Give the preparation type.
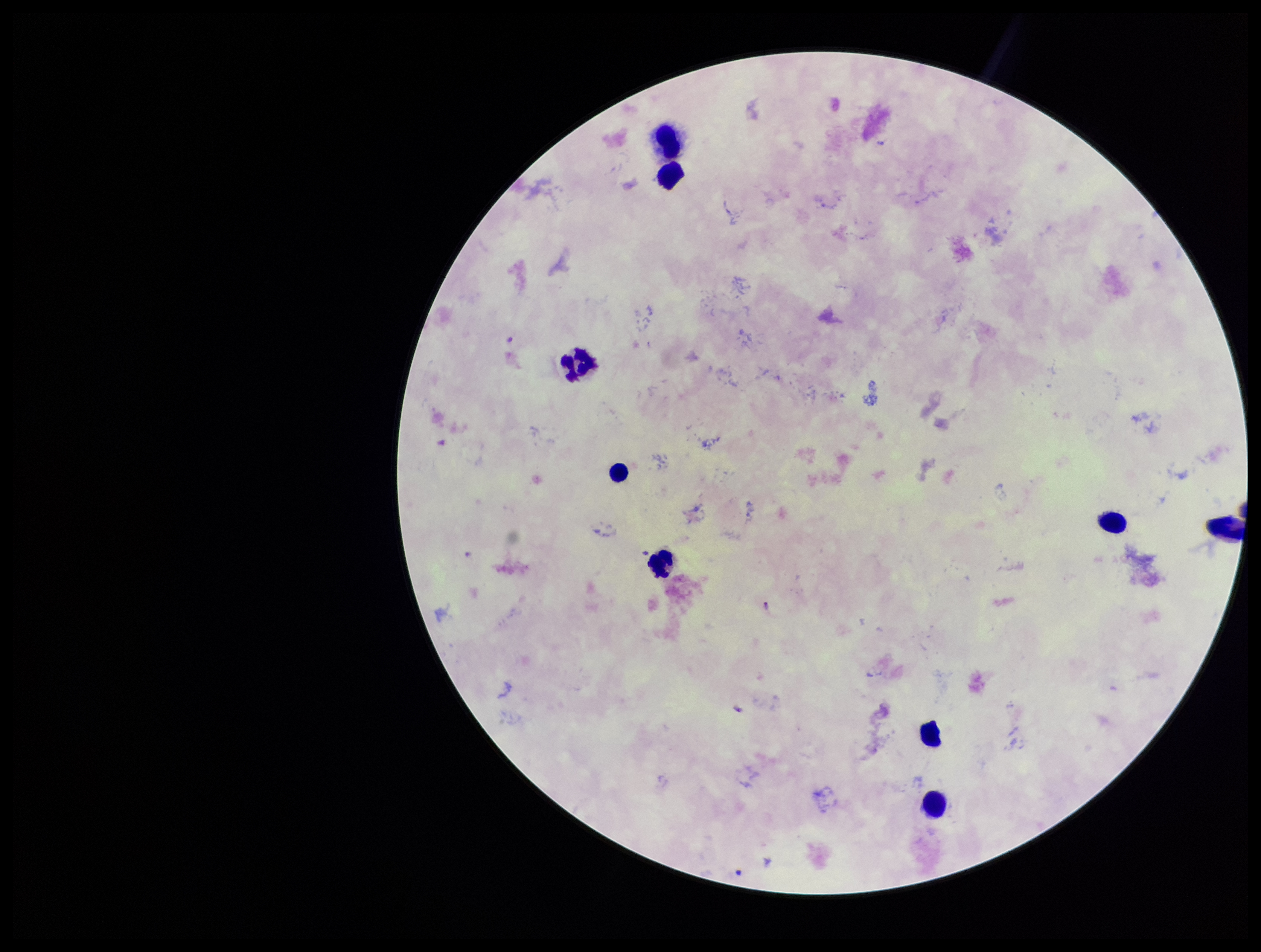
Thick.

Parasite count: 1. Species reported for this patient: Plasmodium falciparum. Patient malaria status: positive. One field from this slide. Smartphone photograph taken through the eyepiece of a microscope. Plasmodium parasites: identified. Leukocyte count: 9. Stained with Giemsa. Image is 1261×952 pixels.